Give the extent of all Plasmodium falciparum-infected red blood cells.
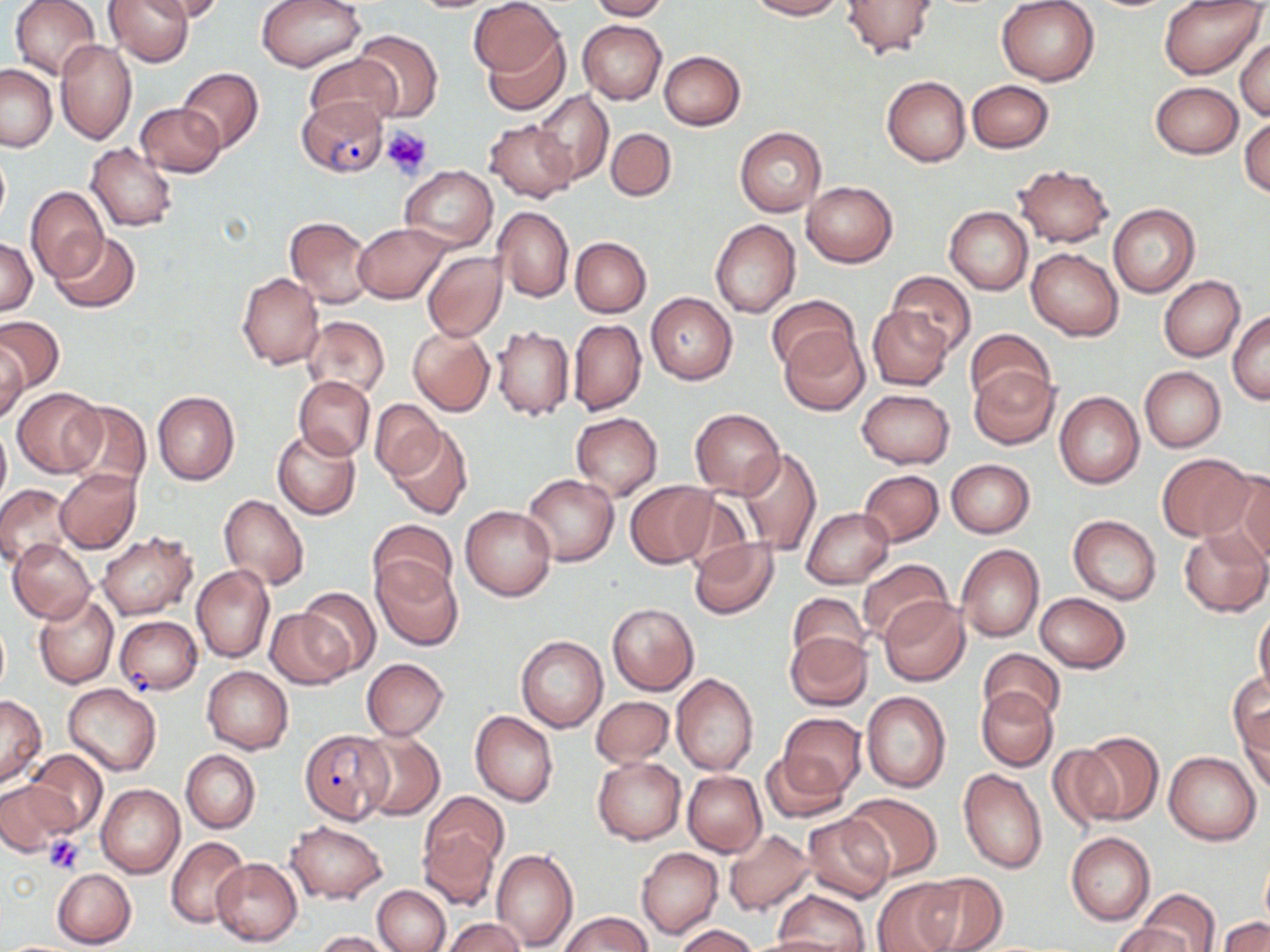

Approximate bounding boxes as (x1,y1)-(x2,y2) corner pairs in pixels.
Plasmodium falciparum-infected red blood cells: (296,98)-(389,177), (115,616)-(202,695), (299,729)-(390,823).

Summary:
  - Uninfected red blood cell locations: (10,0)-(103,80), (105,0)-(193,66), (143,0)-(225,21), (257,0)-(365,71), (470,0)-(560,80), (588,0)-(668,21), (749,0)-(844,20), (842,0)-(938,59), (1160,0)-(1266,78), (407,1)-(499,13), (996,1)-(1100,85), (579,20)-(666,104), (353,29)-(443,121), (482,33)-(567,115), (1236,37)-(1270,120), (55,39)-(137,143), (659,51)-(746,130), (305,54)-(401,132), (0,64)-(57,152), (178,68)-(263,153), (882,76)-(971,167), (966,80)-(1054,152), (1149,81)-(1243,158), (532,90)-(614,185), (136,103)-(225,177), (1240,117)-(1269,197), (484,119)-(577,204), (735,127)-(826,216), (606,128)-(676,200), (87,143)-(178,231), (0,144)-(10,233), (1013,164)-(1114,248), (401,165)-(498,251), (803,181)-(898,267), (26,187)-(108,283), (1108,204)-(1199,297), (945,206)-(1033,294), (492,207)-(574,303), (284,215)-(376,309), (710,219)-(800,318), (354,223)-(449,303), (49,232)-(140,313), (570,237)-(651,317), (1,239)-(37,315), (1026,247)-(1124,341), (422,251)-(507,342), (889,272)-(976,356), (237,273)-(324,370), (1159,276)-(1245,361), (646,293)-(737,384), (766,295)-(859,374), (867,305)-(953,391), (1229,311)-(1270,403), (0,315)-(64,394), (301,315)-(390,399), (568,319)-(646,416), (492,326)-(575,421), (407,328)-(495,416), (779,329)-(869,414), (964,329)-(1055,408), (0,342)-(28,426), (1139,366)-(1225,452), (969,367)-(1058,448), (295,375)-(375,459), (13,388)-(106,477), (856,389)-(955,469), (152,391)-(240,486), (1055,392)-(1145,489), (62,399)-(151,494), (369,399)-(445,481), (689,407)-(784,498), (571,412)-(662,501), (0,421)-(10,510), (389,426)-(471,520), (273,429)-(361,519), (736,448)-(821,556), (1155,453)-(1255,541), (945,459)-(1035,537), (56,469)-(140,554), (858,469)-(945,546), (1222,470)-(1270,564), (523,474)-(618,566), (626,482)-(714,568), (0,484)-(72,567), (676,490)-(755,571), (218,494)-(309,593), (461,504)-(556,600), (802,507)-(894,588), (1069,516)-(1161,604), (368,518)-(457,600), (1179,528)-(1269,617), (96,531)-(198,619), (9,538)-(95,624), (689,538)-(778,620), (957,544)-(1044,642), (856,558)-(953,644), (373,559)-(462,650), (192,565)-(274,662), (298,588)-(380,677), (788,592)-(869,669), (1036,593)-(1130,673), (33,594)-(118,688), (879,598)-(969,686), (607,603)-(698,695), (265,608)-(354,688), (1254,609)-(1270,698), (784,631)-(872,711), (516,635)-(607,733), (977,648)-(1065,723), (360,658)-(449,740), (202,666)-(293,753), (672,674)-(760,776), (1229,674)-(1270,759), (63,683)-(162,776), (978,686)-(1058,770), (861,691)-(951,793), (0,696)-(45,785), (592,696)-(674,767), (1237,706)-(1270,793), (470,710)-(558,807), (777,714)-(866,798), (357,730)-(444,820), (1076,733)-(1163,825), (1047,745)-(1122,831), (180,749)-(259,833), (26,750)-(108,835), (1163,750)-(1262,845), (759,751)-(847,825), (592,755)-(686,844), (958,767)-(1047,874), (683,771)-(765,856), (0,781)-(74,857), (96,783)-(186,877), (423,791)-(507,873), (842,793)-(942,880), (802,813)-(895,903), (284,820)-(387,904), (723,828)-(818,916), (418,829)-(498,911), (1066,832)-(1155,924), (167,836)-(251,930), (637,847)-(723,939), (491,849)-(578,951), (1260,856)-(1270,929), (212,857)-(302,945), (52,868)-(136,949), (913,871)-(1007,952), (873,878)-(961,952), (372,885)-(450,952), (773,891)-(870,952), (1139,891)-(1220,952), (561,912)-(651,952), (1219,915)-(1269,952), (441,918)-(526,952), (1113,923)-(1193,952), (674,925)-(758,952), (314,930)-(393,952), (744,935)-(855,952)
  - Platelet locations: (382,125)-(433,179), (45,835)-(85,874)
  - Slide-level diagnosis: Plasmodium falciparum
  - Image size: 1270×952 pixels
  - Modality: optical microscopy
  - Magnification: 1000x
  - Preparation: thin blood film
  - Field of view: single
  - Stain: May-Grünwald-Giemsa